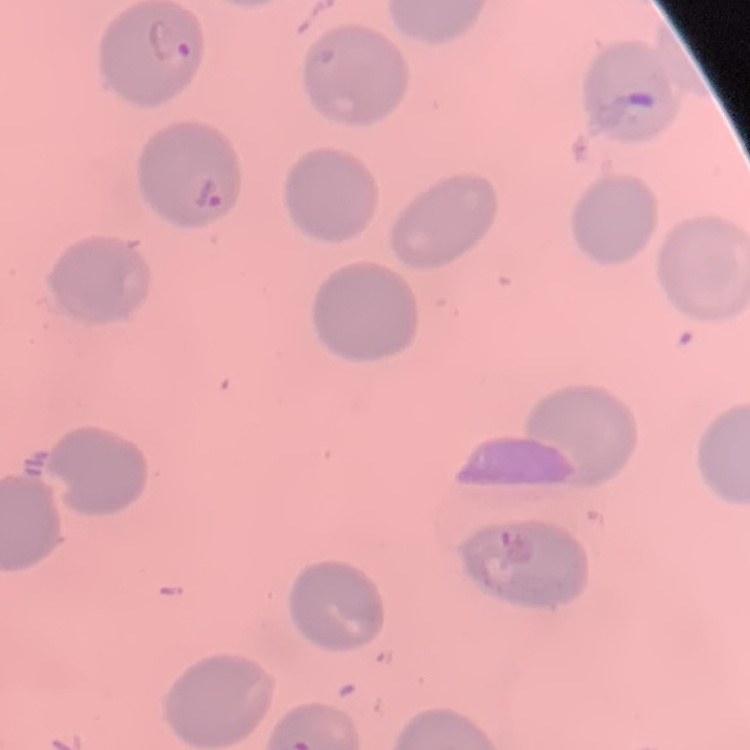
erythrocyte_morphology: no rouleaux formation
preparation: thin blood film
stain: Field's or Giemsa
image_type: one tile cut from a larger photomicrograph